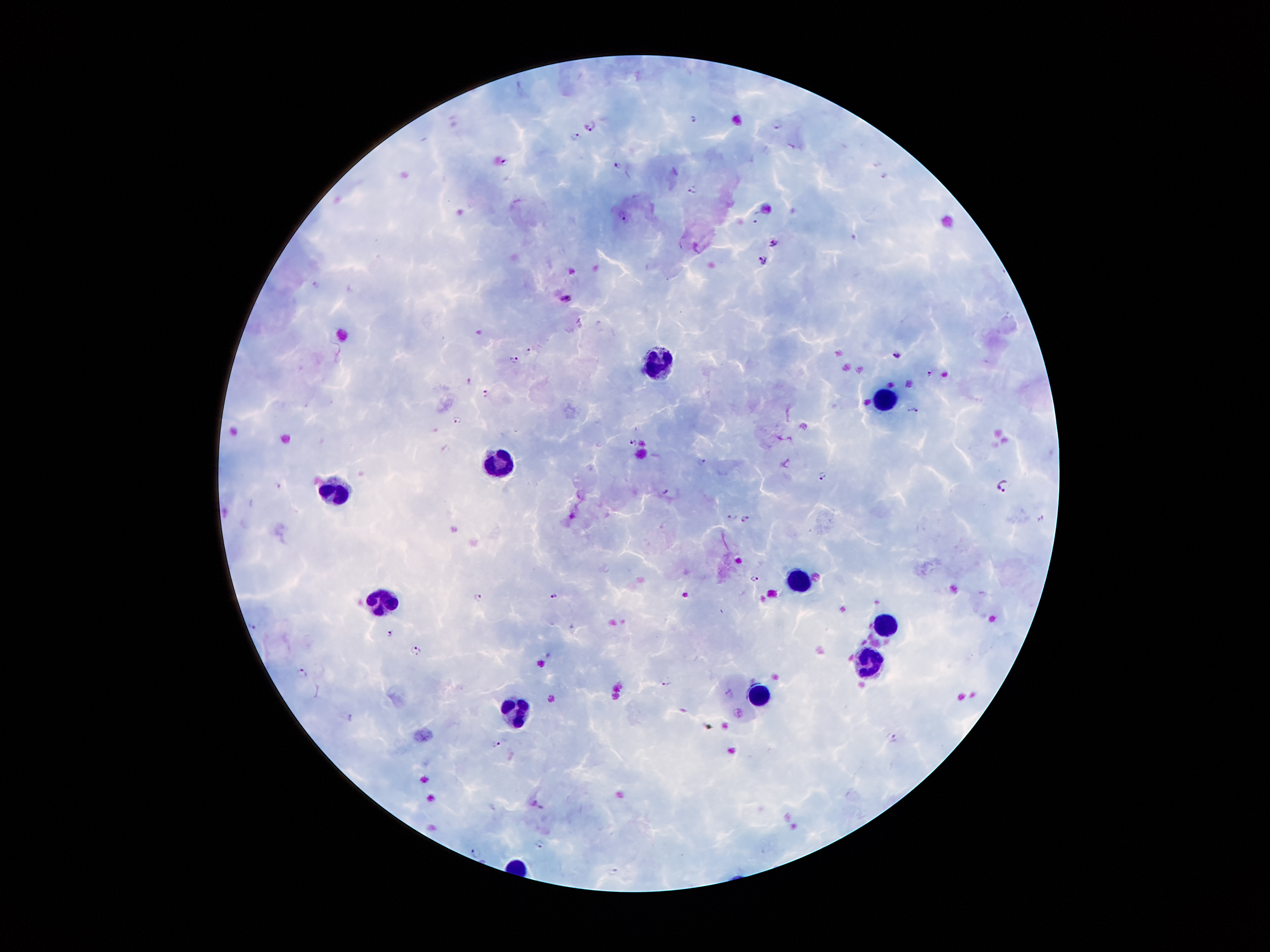 Approximate centers as (x, y) in pixels. Leukocyte locations: (656, 363), (886, 404), (503, 463), (343, 496), (796, 580), (388, 600), (884, 625), (867, 664), (762, 694), (519, 714). Malaria parasite locations: (692, 118), (592, 125), (777, 125), (576, 136), (504, 163), (618, 164), (885, 175), (693, 189), (624, 216), (758, 216), (772, 243), (764, 261), (315, 281), (565, 298), (528, 351), (898, 355), (513, 358), (929, 373), (470, 382), (485, 393), (912, 410), (457, 419), (632, 441), (702, 461), (822, 475), (1003, 485), (733, 517), (746, 518), (756, 578), (554, 595), (478, 597), (253, 625), (393, 632), (416, 651), (302, 672), (668, 681), (346, 716), (894, 738), (497, 744), (538, 844), (476, 853), (611, 871). Photographed through the microscope eyepiece with a smartphone camera. 100x magnification. Patient malaria status: positive for Plasmodium falciparum. Giemsa stain. Thick blood smear. Image is 1270×952 pixels. One field from this slide.